Report the malaria status of this cell.
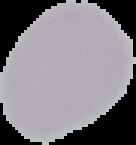
It is uninfected.

Summary:
  - Image size: 136×145 pixels
  - Preparation: thin blood smear
  - Image type: segmented cell region on a black background